Classify this cell by malaria status.
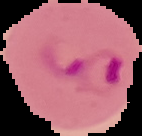
Parasitized.

image type = segmented cell region with the area outside set to black
preparation = thin blood smear
image size = 142×136 pixels